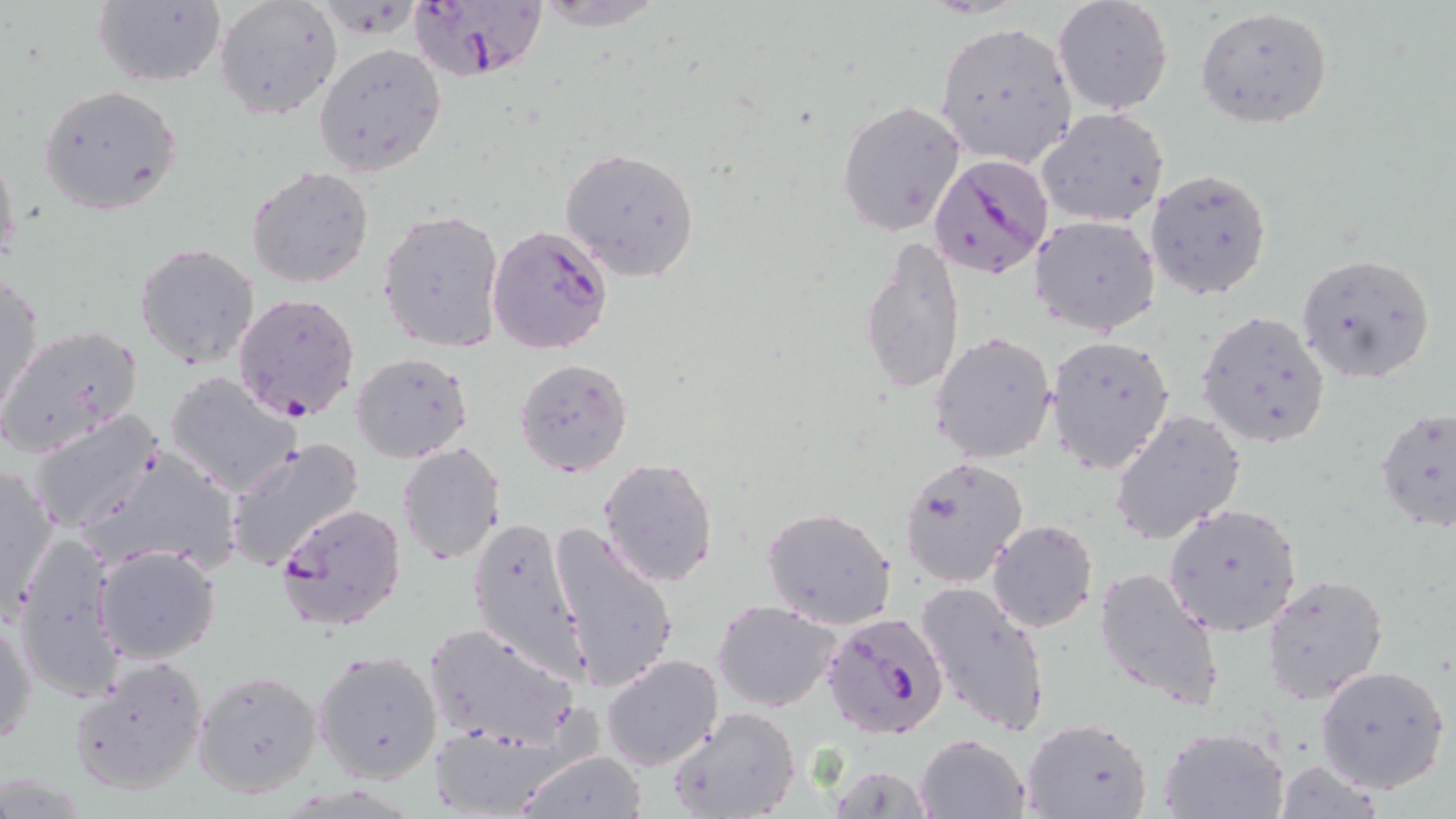

Approximate bounding boxes as (x1,y1)-(x2,y2) corner pairs in pixels. Plasmodium falciparum-infected red blood cell locations: (408,1)-(548,81), (928,153)-(1053,279), (486,224)-(614,353), (232,292)-(361,422), (275,502)-(407,632), (822,612)-(948,740). Uninfected red blood cell locations: (214,0)-(340,120), (1052,0)-(1174,115), (91,1)-(226,88), (529,2)-(670,31), (1195,6)-(1333,129), (933,20)-(1077,169), (314,43)-(447,178), (38,84)-(181,216), (836,100)-(965,235), (1036,106)-(1168,228), (0,145)-(21,274), (560,147)-(701,280), (247,165)-(374,288), (1145,167)-(1273,300), (379,207)-(506,351), (1031,215)-(1160,337), (860,233)-(967,397), (135,242)-(260,370), (1296,251)-(1436,385), (1,275)-(44,421), (1195,309)-(1332,449), (0,323)-(145,456), (929,329)-(1058,463), (1045,334)-(1176,475), (351,352)-(473,462), (514,358)-(633,477), (165,372)-(304,497), (1375,406)-(1456,532), (1111,408)-(1245,545), (27,410)-(166,535), (226,436)-(363,571), (397,441)-(506,565), (81,446)-(241,574), (900,455)-(1029,587), (598,457)-(721,588), (0,463)-(60,621), (1163,501)-(1303,637), (762,505)-(898,630), (467,516)-(590,683), (988,519)-(1098,634), (550,524)-(680,695), (12,532)-(130,702), (93,544)-(220,665), (1092,566)-(1224,708), (1261,571)-(1389,705), (914,581)-(1051,738), (712,600)-(842,712), (1,609)-(36,751), (421,622)-(579,751), (315,652)-(441,785), (601,654)-(723,772), (67,655)-(209,796), (1316,664)-(1450,793), (194,669)-(323,798), (668,706)-(801,819), (1019,716)-(1153,819), (426,722)-(566,818), (1158,727)-(1287,818), (915,734)-(1028,818), (513,750)-(648,819), (1277,758)-(1384,818), (825,765)-(936,818). Slide-level diagnosis: Plasmodium falciparum. May-Grünwald-Giemsa-stained preparation. Thin blood film. Image is 1456×819 pixels. Light microscopy. Single field of view. 1000x magnification.